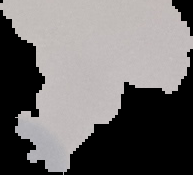

Summary:
  - Preparation: thin blood film
  - Result: no malaria parasites seen
  - Image size: 193×175 pixels
  - Image type: segmented cell region on a black background